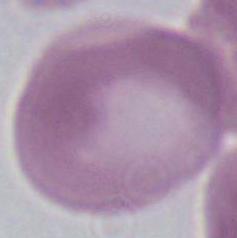 Captured at 1000x magnification. Photomicrograph. A red blood cell is seen.